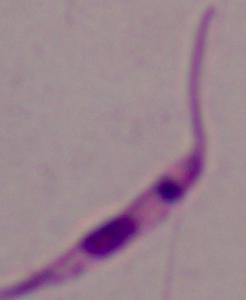

A Leishmania parasite is shown. 1000x magnification. Micrograph.